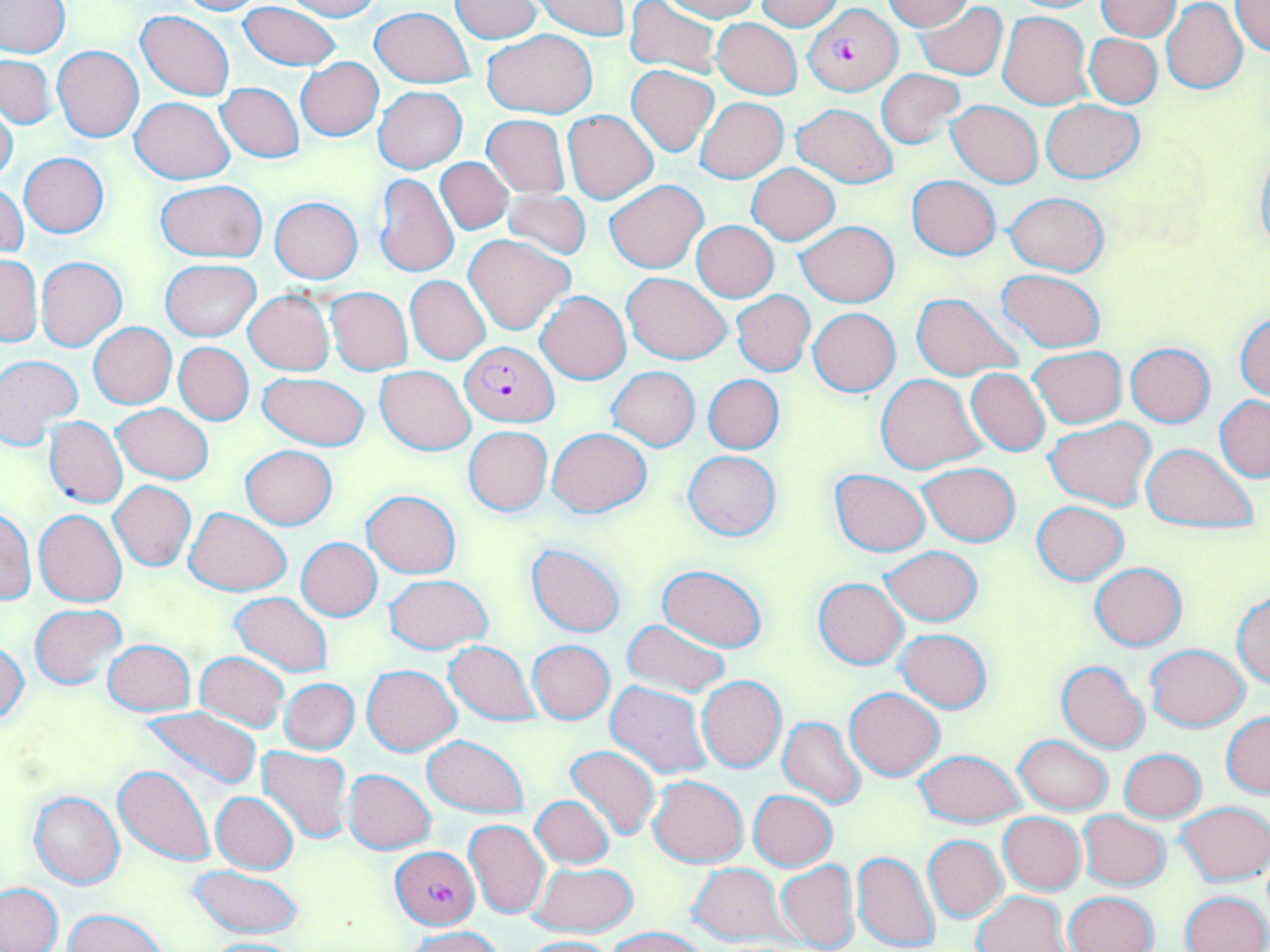

Approximate bounding boxes as [x1, y1, x2, y2] in pixels. Plasmodium falciparum-infected red blood cell locations: [803, 5, 903, 95], [460, 341, 559, 427], [390, 846, 479, 929]. Uninfected red blood cell locations: [1, 0, 70, 56], [172, 0, 263, 15], [281, 0, 382, 21], [449, 0, 544, 42], [625, 0, 723, 79], [656, 0, 762, 20], [755, 0, 846, 29], [883, 0, 972, 31], [1098, 0, 1179, 40], [1231, 0, 1270, 56], [532, 1, 631, 38], [240, 2, 343, 72], [916, 2, 1007, 80], [1162, 3, 1247, 94], [369, 6, 475, 86], [135, 10, 235, 100], [997, 11, 1091, 109], [712, 19, 802, 98], [482, 29, 597, 118], [1084, 33, 1162, 108], [53, 45, 143, 142], [0, 54, 58, 127], [295, 58, 383, 140], [627, 65, 718, 156], [877, 70, 964, 149], [216, 82, 304, 162], [375, 86, 466, 173], [130, 96, 235, 183], [695, 97, 788, 183], [0, 98, 19, 186], [1042, 99, 1144, 184], [947, 100, 1043, 187], [792, 103, 898, 188], [564, 111, 657, 202], [483, 115, 570, 197], [19, 153, 109, 238], [1255, 153, 1270, 257], [435, 159, 513, 233], [747, 164, 839, 244], [373, 172, 460, 277], [907, 175, 1001, 260], [605, 179, 708, 273], [155, 180, 268, 262], [1, 182, 28, 260], [499, 189, 591, 259], [1004, 193, 1108, 274], [270, 197, 363, 284], [691, 220, 778, 301], [796, 220, 898, 307], [464, 234, 572, 333], [0, 255, 42, 346], [36, 256, 126, 350], [161, 259, 261, 341], [997, 268, 1106, 352], [622, 272, 731, 363], [406, 276, 491, 364], [326, 287, 412, 376], [244, 291, 334, 376], [537, 291, 630, 384], [731, 291, 815, 376], [911, 292, 1023, 380], [809, 308, 900, 395], [1234, 314, 1270, 401], [89, 323, 177, 409], [174, 342, 254, 424], [1126, 342, 1214, 427], [1028, 346, 1125, 428], [0, 353, 82, 450], [375, 366, 474, 454], [608, 367, 700, 450], [966, 369, 1050, 455], [257, 372, 368, 450], [702, 374, 783, 454], [876, 374, 983, 474], [1215, 396, 1270, 480], [112, 403, 212, 483], [44, 416, 127, 508], [1046, 417, 1156, 510], [463, 426, 553, 516], [547, 428, 651, 516], [1142, 443, 1258, 532], [241, 445, 337, 530], [683, 450, 779, 541], [918, 463, 1019, 545], [830, 469, 930, 555], [108, 481, 197, 571], [361, 490, 460, 577], [1032, 501, 1127, 584], [185, 507, 292, 595], [1, 508, 36, 605], [34, 509, 127, 606], [296, 537, 381, 620], [527, 542, 625, 637], [880, 546, 983, 624], [1090, 562, 1187, 649], [657, 564, 765, 651], [384, 574, 491, 653], [814, 578, 908, 669], [1232, 591, 1270, 689], [231, 592, 332, 676], [30, 604, 126, 689], [621, 619, 730, 697], [897, 629, 991, 711], [103, 639, 193, 716], [0, 640, 30, 727], [444, 640, 538, 725], [528, 640, 615, 723], [1146, 644, 1249, 730], [196, 652, 289, 729], [1057, 660, 1150, 752], [361, 664, 461, 755], [697, 675, 785, 772], [281, 678, 359, 754], [605, 681, 711, 780], [845, 687, 945, 780], [142, 706, 261, 791], [1221, 711, 1270, 796], [778, 716, 865, 809], [423, 734, 529, 817], [1015, 736, 1112, 814], [564, 745, 661, 841], [257, 746, 351, 843], [1119, 749, 1206, 822], [915, 750, 1026, 826], [114, 764, 216, 867], [344, 769, 436, 853], [648, 775, 747, 867], [29, 790, 124, 889], [748, 790, 837, 870], [212, 791, 299, 874], [531, 796, 614, 868], [1178, 802, 1269, 885], [1076, 810, 1170, 890], [997, 812, 1087, 894], [464, 819, 550, 918], [924, 835, 1006, 921], [852, 850, 940, 951], [775, 859, 859, 951], [528, 863, 637, 935], [189, 864, 304, 938], [689, 864, 789, 945], [0, 884, 65, 951], [974, 890, 1072, 952], [1182, 891, 1269, 952], [1063, 892, 1157, 952], [65, 910, 170, 952], [608, 925, 709, 952], [407, 926, 503, 952], [192, 937, 308, 951], [519, 937, 620, 952]. Slide-level diagnosis: Plasmodium falciparum. Single field of view. May-Grünwald-Giemsa-stained preparation. Thin blood smear. Captured at 1000x magnification. Light microscopy. Image is 1270×952 pixels.